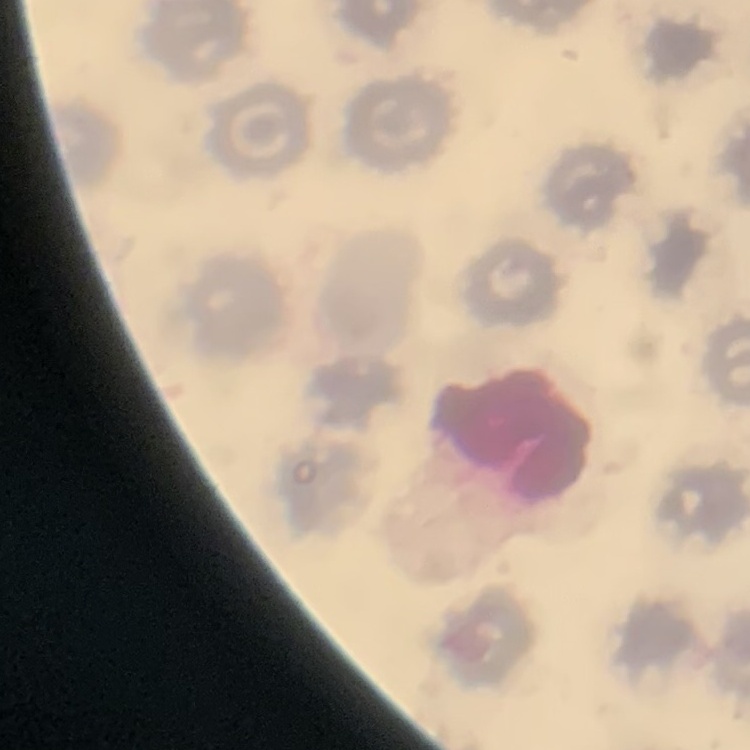

red blood cell morphology = no rouleaux formation
preparation = thin blood film
image type = square crop of a larger photomicrograph
stain = Field's or Giemsa